Classify this cell by malaria status.
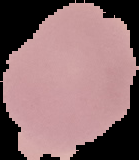
Uninfected.

From a thin blood smear. The area outside the segmented cell region is set to black. Image is 139×160 pixels.